Name the cell type shown.
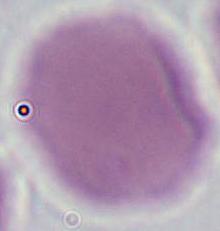
An erythrocyte.

magnification: 1000x
modality: photomicrograph